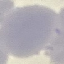

Summary:
  - Result: no malaria parasites seen
  - Capture: smartphone camera at the microscope eyepiece
  - Stain: Giemsa
  - Image type: cell patch, automatically extracted from a larger field of view and resized to 64 × 64 pixels
  - Preparation: thin blood film